Comment on the morphology of the red blood cells.
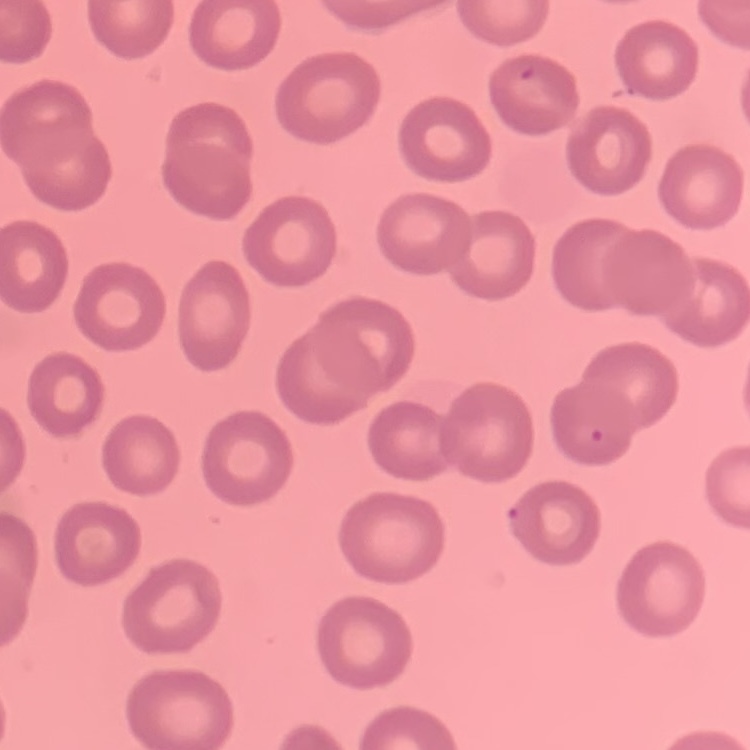

They show no rouleaux formation.

stain = Field's or Giemsa
image type = one tile cut from a larger photomicrograph
preparation = thin blood film